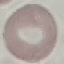

Summary:
  - Malaria status: uninfected
  - Preparation: thin blood smear
  - Stain: Giemsa
  - Image type: automatically extracted cell patch, resized to 64 × 64 pixels
  - Capture: smartphone through the microscope eyepiece